Locate every malaria parasite.
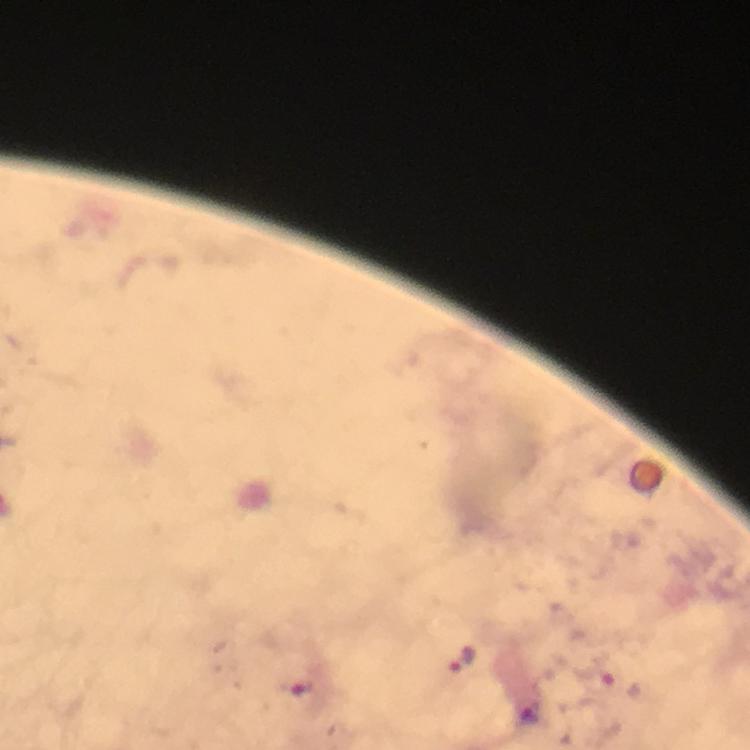
Approximate centers as {x, y} in pixels.
Malaria parasites: {462, 660}, {531, 710}.

Giemsa stain. From a diagnostic examination for malaria. 100x magnification. Immersion oil was used. Photographed with a smartphone mounted on the microscope. Cropped region of a single field of view. Image is 750×750 pixels. Thick blood smear.